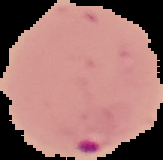 Image is 163×160 pixels. From a thin blood smear. Result: Plasmodium parasites identified. Segmented cell region on a black background.